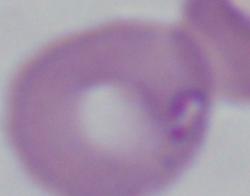
Summary:
  - Modality: micrograph
  - Identification: Babesia
  - Magnification: 1000x